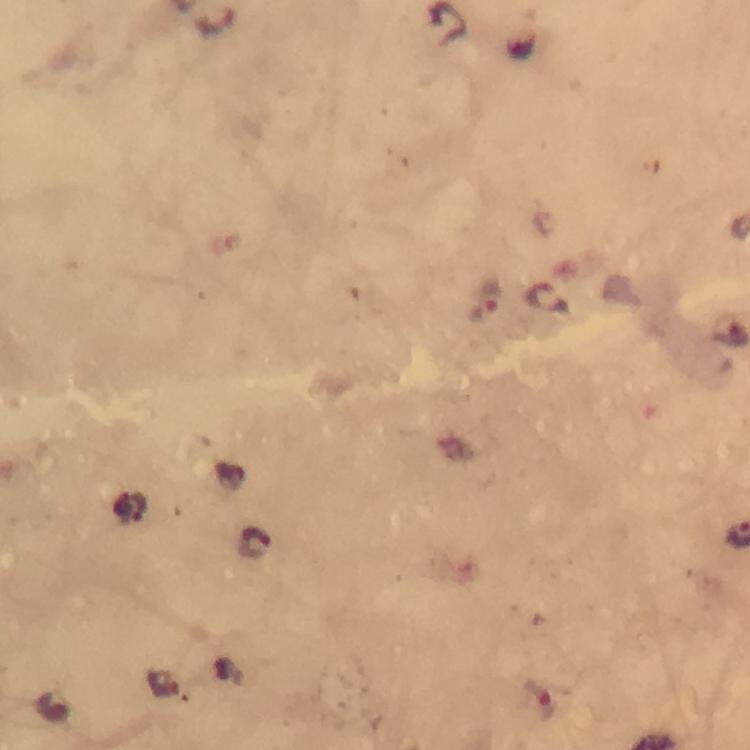

Approximate centers as {x, y} in pixels.
Summary:
  - Malaria parasite locations: {486, 302}, {730, 332}, {130, 508}, {253, 543}, {541, 701}
  - Stain: Giemsa
  - Image size: 750×750 pixels
  - Preparation: thick blood smear
  - Immersion oil: applied
  - Capture: smartphone photograph through a microscope
  - Cropped from: a single field of view
  - Magnification: 100x
  - Context: from a diagnostic examination for malaria